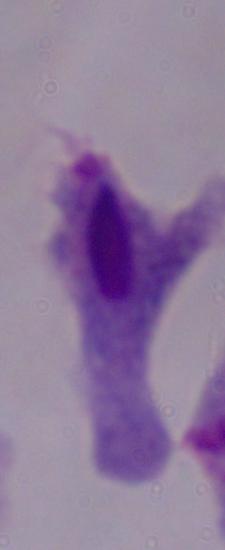

1000x magnification. A trichomonad is seen. Photomicrograph.